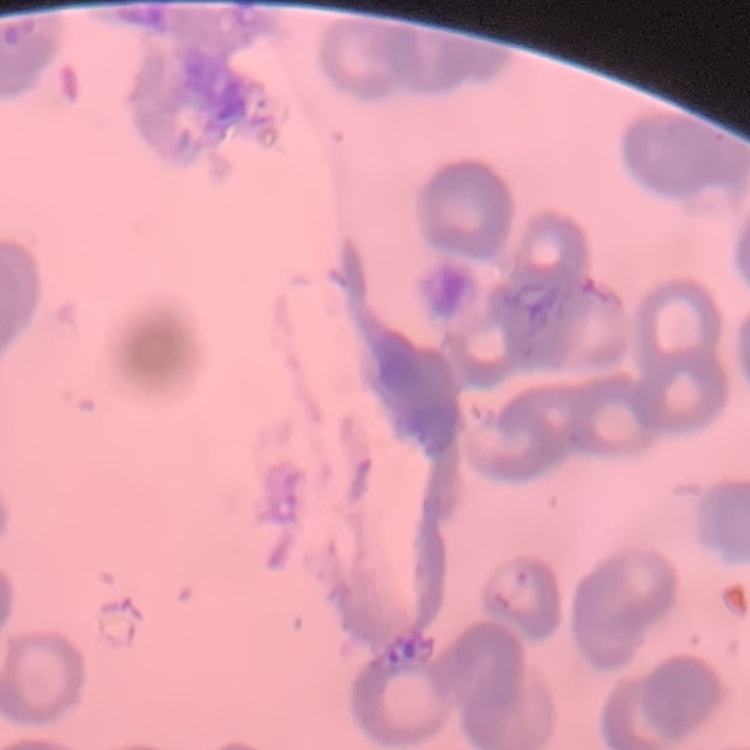
Summary:
  - Red blood cell morphology: rouleaux formation
  - Stain: Field's or Giemsa
  - Image type: one tile cut from a larger photomicrograph
  - Preparation: thin blood film